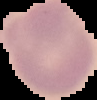

image_size: 97×100 pixels
result: negative for malaria parasites
image_type: cell region segmented out of the field of view; surrounding area masked to black
preparation: thin blood film